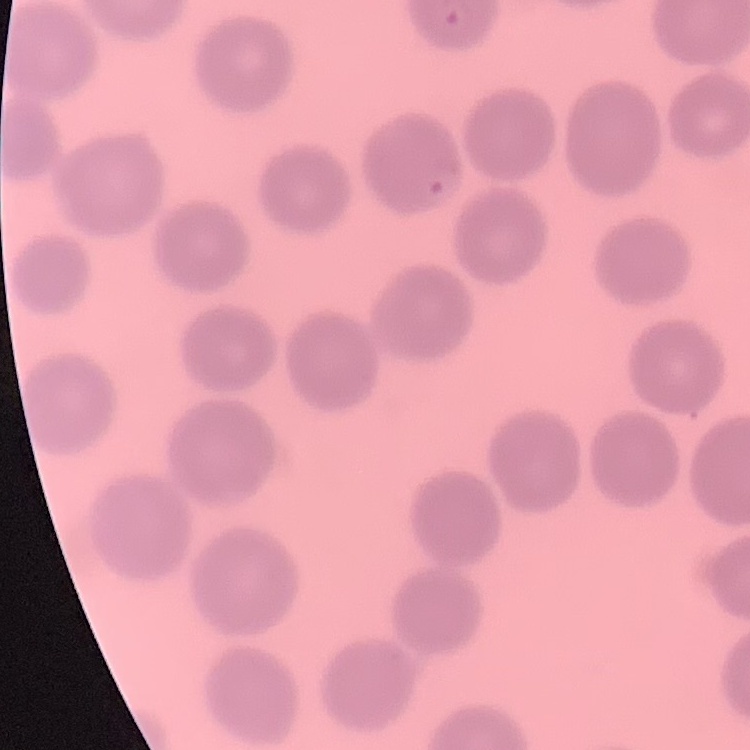

erythrocyte morphology = no rouleaux formation
preparation = thin blood smear
stain = Field's or Giemsa
image type = square crop of a larger photomicrograph